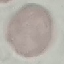

Result: no malaria parasites seen. Thin blood smear. Automatically extracted cell patch, resized to 64 × 64 pixels. Giemsa stain. Acquired by smartphone through the microscope eyepiece.